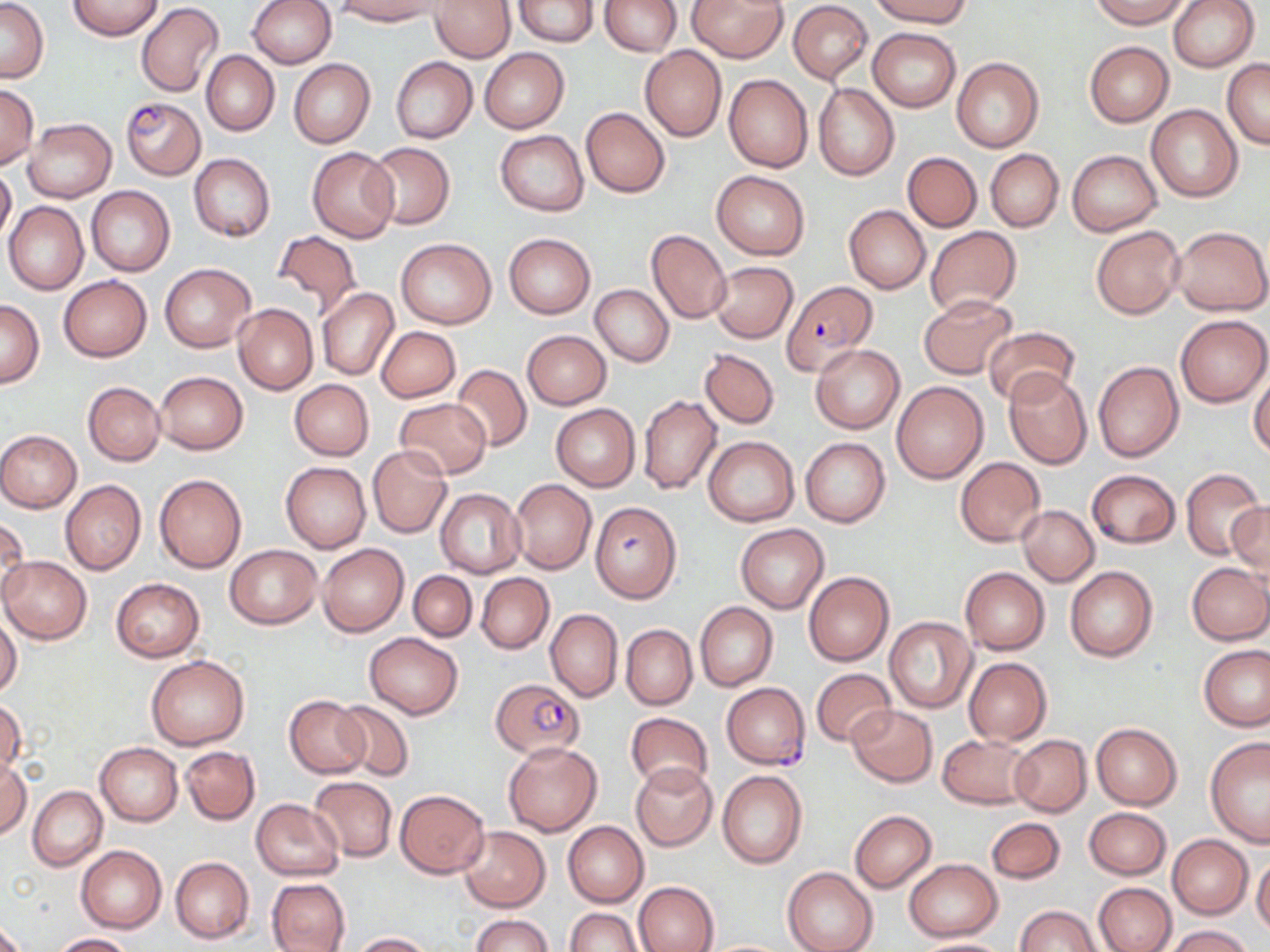

Approximate bounding boxes as [x1, y1, x2, y2] in pixels. Uninfected red blood cell locations: [1, 0, 48, 82], [67, 0, 163, 40], [247, 0, 336, 68], [334, 0, 440, 25], [432, 0, 514, 62], [514, 0, 598, 46], [601, 0, 681, 55], [688, 0, 786, 62], [872, 0, 974, 26], [1090, 0, 1189, 27], [1168, 0, 1259, 72], [788, 1, 873, 84], [136, 3, 225, 99], [868, 27, 961, 111], [1084, 42, 1173, 127], [640, 45, 727, 141], [480, 48, 570, 133], [202, 51, 280, 135], [951, 56, 1045, 152], [390, 57, 477, 143], [1223, 57, 1269, 148], [288, 58, 376, 149], [724, 74, 813, 173], [813, 82, 899, 180], [0, 84, 39, 168], [1146, 104, 1243, 202], [581, 107, 670, 198], [24, 118, 116, 202], [496, 130, 588, 215], [364, 142, 455, 229], [307, 146, 399, 243], [986, 149, 1063, 231], [1067, 150, 1161, 236], [902, 152, 981, 230], [188, 153, 275, 241], [0, 165, 15, 245], [711, 171, 810, 259], [87, 186, 174, 276], [4, 202, 89, 295], [844, 205, 931, 294], [1173, 225, 1270, 316], [926, 226, 1021, 314], [1091, 226, 1185, 319], [645, 229, 731, 324], [274, 230, 361, 317], [504, 233, 594, 318], [396, 238, 496, 328], [709, 261, 798, 344], [161, 263, 256, 352], [57, 276, 152, 362], [590, 285, 673, 367], [317, 288, 398, 381], [918, 294, 1017, 379], [1, 298, 44, 387], [232, 303, 318, 395], [1176, 315, 1270, 408], [983, 325, 1079, 406], [376, 326, 460, 403], [521, 330, 612, 409], [811, 343, 904, 434], [700, 348, 781, 429], [1092, 361, 1184, 463], [451, 364, 533, 452], [1002, 370, 1092, 469], [155, 371, 248, 453], [1250, 374, 1270, 458], [289, 379, 374, 461], [891, 381, 989, 483], [83, 382, 165, 466], [637, 394, 721, 494], [393, 398, 492, 480], [551, 404, 640, 492], [0, 429, 81, 512], [704, 436, 799, 526], [801, 437, 890, 527], [368, 445, 452, 538], [955, 456, 1047, 548], [280, 461, 370, 553], [1180, 467, 1268, 561], [1086, 470, 1181, 548], [154, 474, 246, 573], [509, 479, 596, 574], [60, 480, 146, 574], [436, 488, 524, 579], [1228, 499, 1270, 579], [589, 501, 682, 602], [1018, 505, 1099, 586], [1, 516, 29, 606], [735, 524, 829, 612], [318, 543, 408, 636], [225, 544, 321, 628], [1, 557, 91, 644], [1186, 562, 1270, 644], [959, 566, 1050, 655], [1066, 566, 1158, 662], [409, 571, 476, 641], [803, 571, 894, 667], [476, 573, 553, 654], [112, 578, 204, 661], [695, 602, 778, 691], [545, 609, 622, 702], [0, 614, 22, 699], [884, 617, 977, 712], [622, 624, 697, 709], [365, 633, 462, 719], [1198, 645, 1269, 731], [146, 655, 249, 750], [962, 657, 1052, 746], [811, 667, 898, 748], [285, 694, 370, 778], [0, 700, 25, 780], [334, 702, 414, 781], [847, 704, 937, 786], [626, 712, 712, 793], [1092, 723, 1182, 809], [938, 734, 1034, 809], [1009, 734, 1091, 817], [1204, 738, 1270, 848], [502, 742, 601, 836], [95, 743, 182, 825], [179, 746, 260, 825], [1, 758, 31, 840], [630, 763, 717, 851], [718, 771, 807, 869], [309, 777, 397, 862], [27, 786, 107, 871], [394, 788, 490, 879], [251, 799, 343, 880], [1084, 807, 1170, 880], [849, 811, 936, 892], [986, 818, 1065, 885], [564, 821, 648, 907], [459, 826, 550, 912], [1168, 835, 1252, 918], [76, 845, 167, 933], [1251, 856, 1270, 936], [170, 857, 253, 944], [904, 859, 1001, 941], [783, 867, 878, 952], [266, 877, 351, 951], [632, 881, 718, 951], [1092, 882, 1176, 952], [1014, 906, 1102, 951], [566, 907, 641, 952], [471, 914, 552, 951], [0, 920, 25, 952], [1166, 925, 1252, 952], [349, 932, 432, 951], [48, 933, 135, 951], [910, 937, 1012, 951], [703, 939, 791, 951]. Plasmodium falciparum-infected red blood cell locations: [120, 96, 205, 180], [781, 280, 876, 373], [490, 678, 584, 758], [721, 683, 811, 768]. Slide-level diagnosis: Plasmodium falciparum. Thin blood film. One field of a larger specimen. Optical microscopy. May-Grünwald-Giemsa-stained preparation. Image is 1270×952 pixels. Captured at 1000x magnification.